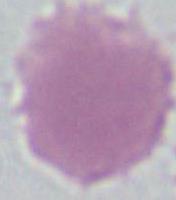

magnification = 1000x
identification = red blood cell
modality = micrograph